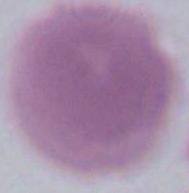
Summary:
  - Identification: red blood cell
  - Magnification: 1000x
  - Modality: micrograph